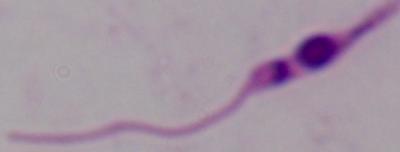 Photomicrograph. 1000x magnification. A Leishmania parasite is seen.